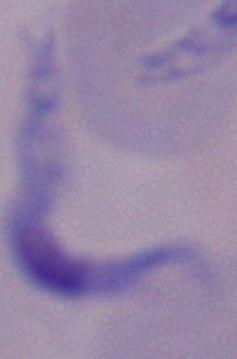

modality = micrograph
identification = trypanosome
magnification = 1000x